Give the position of every malaria parasite.
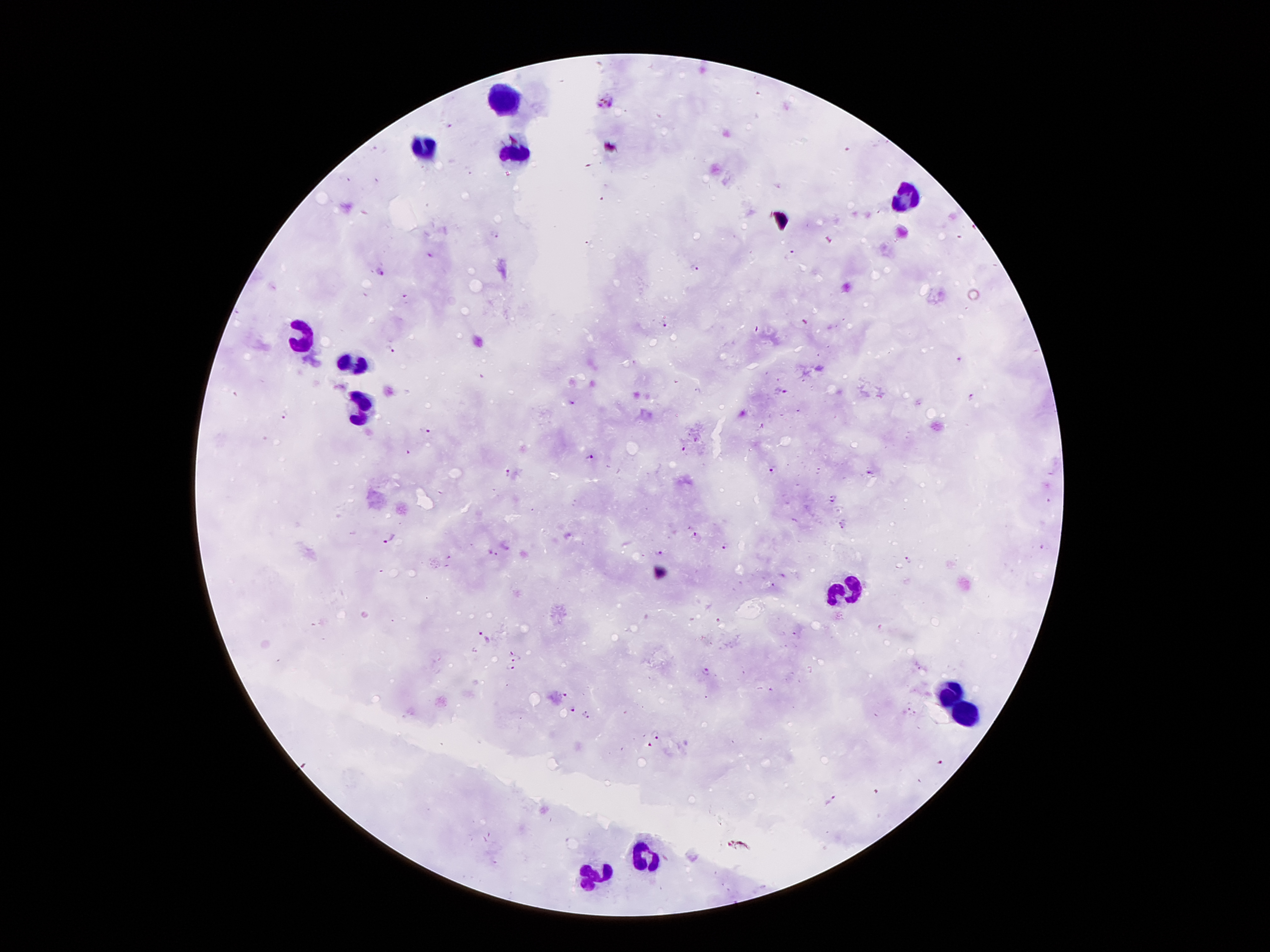

Approximate centers as [x, y] in pixels.
Malaria parasites: [606, 102], [495, 235], [790, 253], [430, 256], [695, 269], [382, 272], [665, 324], [390, 351], [961, 359], [782, 391], [971, 396], [572, 402], [286, 415], [426, 431], [684, 450], [590, 458], [773, 470], [509, 472], [870, 473], [833, 499], [1049, 501], [842, 525], [696, 535], [390, 539], [725, 545], [1042, 548], [658, 552], [494, 554], [449, 557], [907, 560], [773, 584], [794, 634], [485, 639], [513, 651], [518, 658], [920, 666], [510, 667], [705, 670], [567, 695], [573, 708], [907, 709], [584, 710], [915, 714], [588, 718], [656, 734], [652, 745], [941, 762], [830, 802].

image_size: 1270×952 pixels
leukocyte_locations: 'approximate centers as [x, y] in pixels: [505, 97], [425, 152], [516, 156], [905, 201], [303, 340], [354, 363], [362, 412], [845, 590], [948, 692], [966, 711], [647, 856], [593, 875]'
patient_malaria_status: positive for Plasmodium falciparum
magnification: 100x
capture: smartphone through the microscope eyepiece
stain: Giemsa
field_of_view: single
preparation: thick peripheral-blood smear